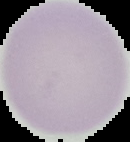

{
  "image_size": "130×142 pixels",
  "result": "no Plasmodium parasites seen",
  "image_type": "segmented cell region on a black background",
  "preparation": "thin blood smear"
}